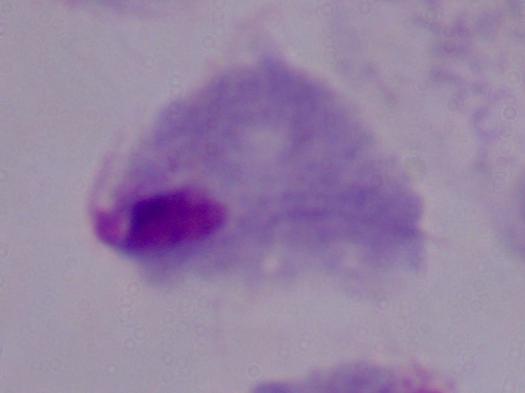
Micrograph. 1000x magnification. A trichomonad is seen.